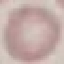
result = negative for malaria parasites
image type = automatically extracted cell patch, resized to 64 × 64 pixels
capture = smartphone camera at the microscope eyepiece
stain = Giemsa
preparation = thin blood smear